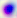

Summary:
  - Identification: Toxoplasma gondii
  - Magnification: 400x
  - Modality: micrograph